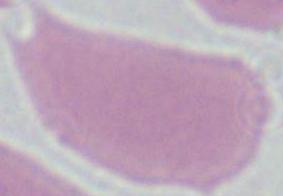

identification = red blood cell
magnification = 1000x
modality = photomicrograph